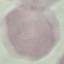

Summary:
  - Result: no malaria parasites detected
  - Stain: Giemsa
  - Capture: smartphone camera at the microscope eyepiece
  - Image type: automatically extracted cell patch, resized to 64 × 64 pixels
  - Preparation: thin blood film